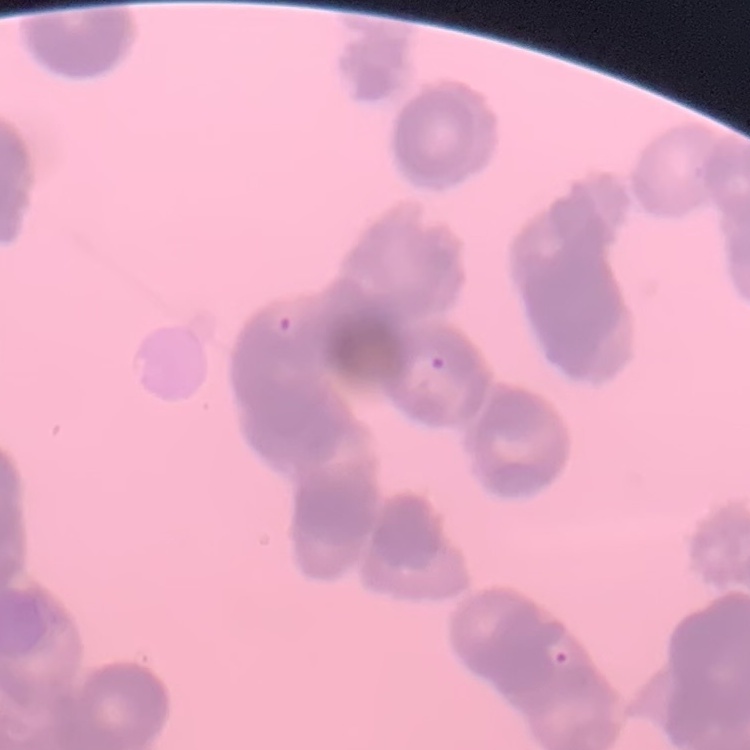 The red blood cells exhibit rouleaux formation. Thin blood film. Square crop of a larger photomicrograph. Field's or Giemsa stain.